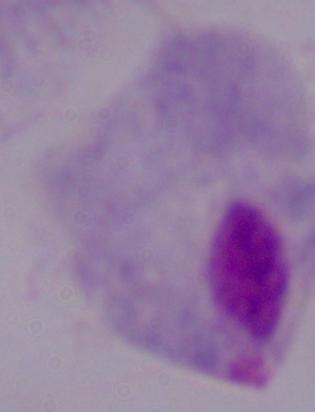

identification = trichomonad
magnification = 1000x
modality = photomicrograph